Classify this cell by malaria status.
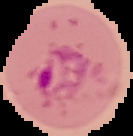
Parasitized.

From a thin blood smear. The area outside the segmented cell region is set to black. Image is 133×136 pixels.